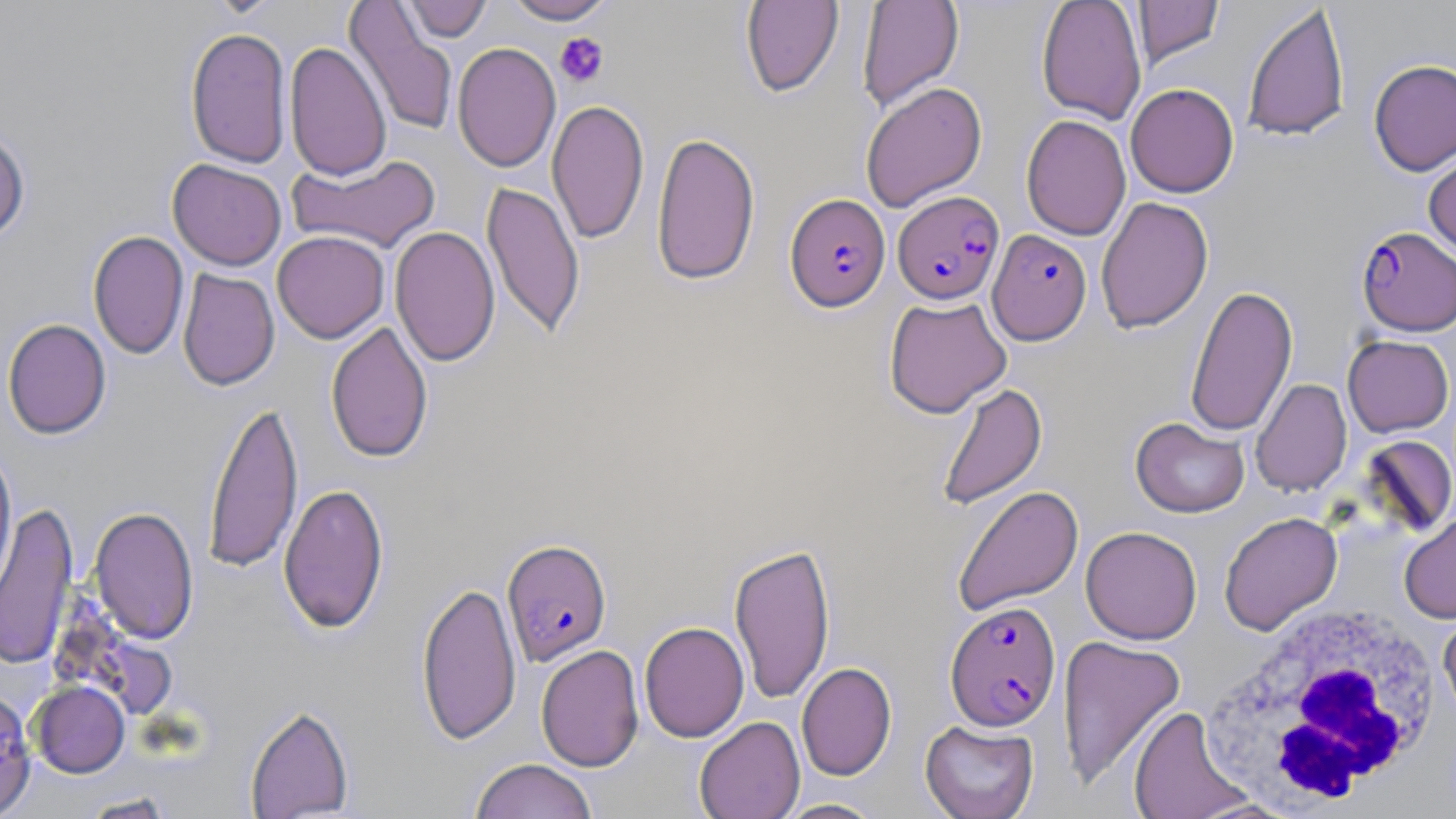

slide-level diagnosis = Plasmodium falciparum
white blood cell locations = approximate bounding boxes as (x1,y1)-(x2,y2) corner pairs in pixels: (1198,599)-(1444,810)
stain = May-Grünwald-Giemsa
uninfected red blood cell locations = approximate bounding boxes as (x1,y1)-(x2,y2) corner pairs in pixels: (399,0)-(492,42), (503,0)-(616,24), (856,0)-(964,113), (1036,0)-(1147,125), (1133,0)-(1224,69), (740,1)-(844,97), (345,2)-(458,138), (1242,4)-(1350,142), (185,26)-(292,169), (284,41)-(391,182), (452,42)-(561,172), (1368,58)-(1456,176), (860,81)-(987,212), (1125,83)-(1239,198), (547,98)-(649,245), (1021,114)-(1131,241), (0,128)-(31,243), (651,130)-(760,286), (1424,147)-(1456,261), (287,154)-(442,254), (167,159)-(287,271), (482,181)-(585,340), (1096,196)-(1214,334), (389,225)-(500,367), (88,230)-(189,360), (272,230)-(390,343), (177,269)-(280,391), (1185,284)-(1297,438), (883,296)-(1012,418), (2,318)-(112,439), (325,320)-(434,463), (1342,334)-(1454,437), (1250,378)-(1352,496), (935,381)-(1047,510), (203,398)-(304,575), (1130,417)-(1250,518), (1356,435)-(1456,538), (0,444)-(17,607), (278,482)-(389,634), (952,485)-(1084,616), (1,502)-(78,670), (89,505)-(200,645), (1399,510)-(1456,624), (1219,511)-(1342,635), (1080,526)-(1202,644), (728,541)-(836,705), (416,579)-(521,745), (1438,609)-(1456,726), (639,621)-(749,742), (1057,634)-(1187,790), (535,644)-(644,771), (797,662)-(896,781), (29,680)-(130,777), (0,687)-(36,819), (245,703)-(354,818), (1128,705)-(1254,819), (694,716)-(805,819), (919,719)-(1040,819), (470,758)-(596,819), (77,792)-(178,818), (775,798)-(885,818)
modality = optical microscopy
Plasmodium falciparum-infected red blood cell locations = approximate bounding boxes as (x1,y1)-(x2,y2) corner pairs in pixels: (893,190)-(1005,305), (785,193)-(890,311), (1356,226)-(1456,336), (987,229)-(1091,345), (501,538)-(612,666), (945,600)-(1061,730)
platelet locations = approximate bounding boxes as (x1,y1)-(x2,y2) corner pairs in pixels: (555,32)-(609,88)
field of view = single
magnification = 1000x
preparation = thin blood smear
image size = 1456×819 pixels